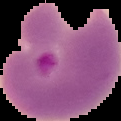
Summary:
  - Malaria status: parasitized
  - Preparation: thin blood film
  - Image size: 121×121 pixels
  - Image type: cell region segmented out of the field of view; surrounding area masked to black